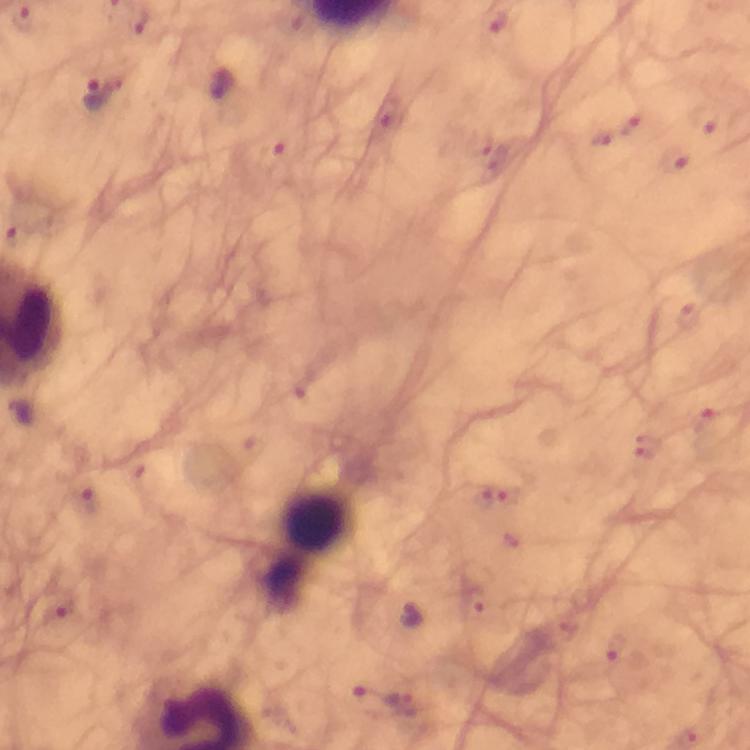
Approximate object centers, in pixels from the top-left corner.
Summary:
  - Leukocyte locations: (x=317, y=519)
  - Malaria parasite locations: (x=23, y=20), (x=141, y=23), (x=221, y=85), (x=106, y=90), (x=632, y=126), (x=602, y=140), (x=86, y=498), (x=60, y=604), (x=411, y=617), (x=404, y=703)
  - Capture: smartphone mounted on the microscope
  - Magnification: 100x
  - Stain: Giemsa
  - Cropped from: a single field of view
  - Context: from a diagnostic examination for malaria
  - Image size: 750×750 pixels
  - Immersion oil: applied
  - Preparation: thick blood smear